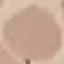
malaria status = uninfected
stain = Giemsa
preparation = thin blood smear
image type = automatically extracted cell patch, resized to 64 × 64 pixels
capture = smartphone through the microscope eyepiece